Comment on the morphology of the red blood cells.
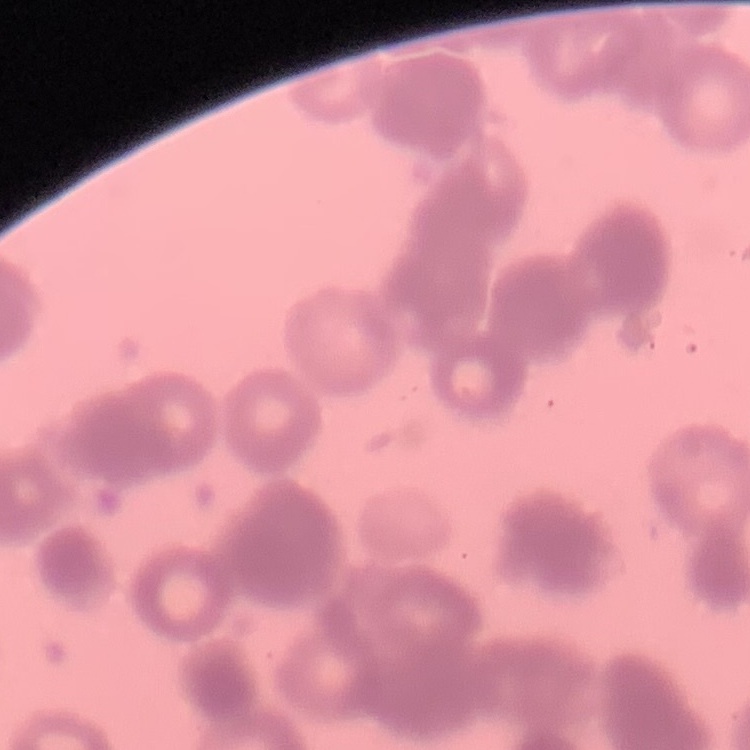
They show rouleaux formation.

Field's or Giemsa stain. Thin blood smear. One tile cut from a larger photomicrograph.